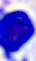
Summary:
  - Magnification: 400x
  - Modality: photomicrograph
  - Identification: leukocyte